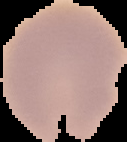
Summary:
  - Result: negative for Plasmodium parasites
  - Preparation: thin blood smear
  - Image type: segmented cell region with the area outside set to black
  - Image size: 127×142 pixels